Point out each Plasmodium parasite and each leukocyte.
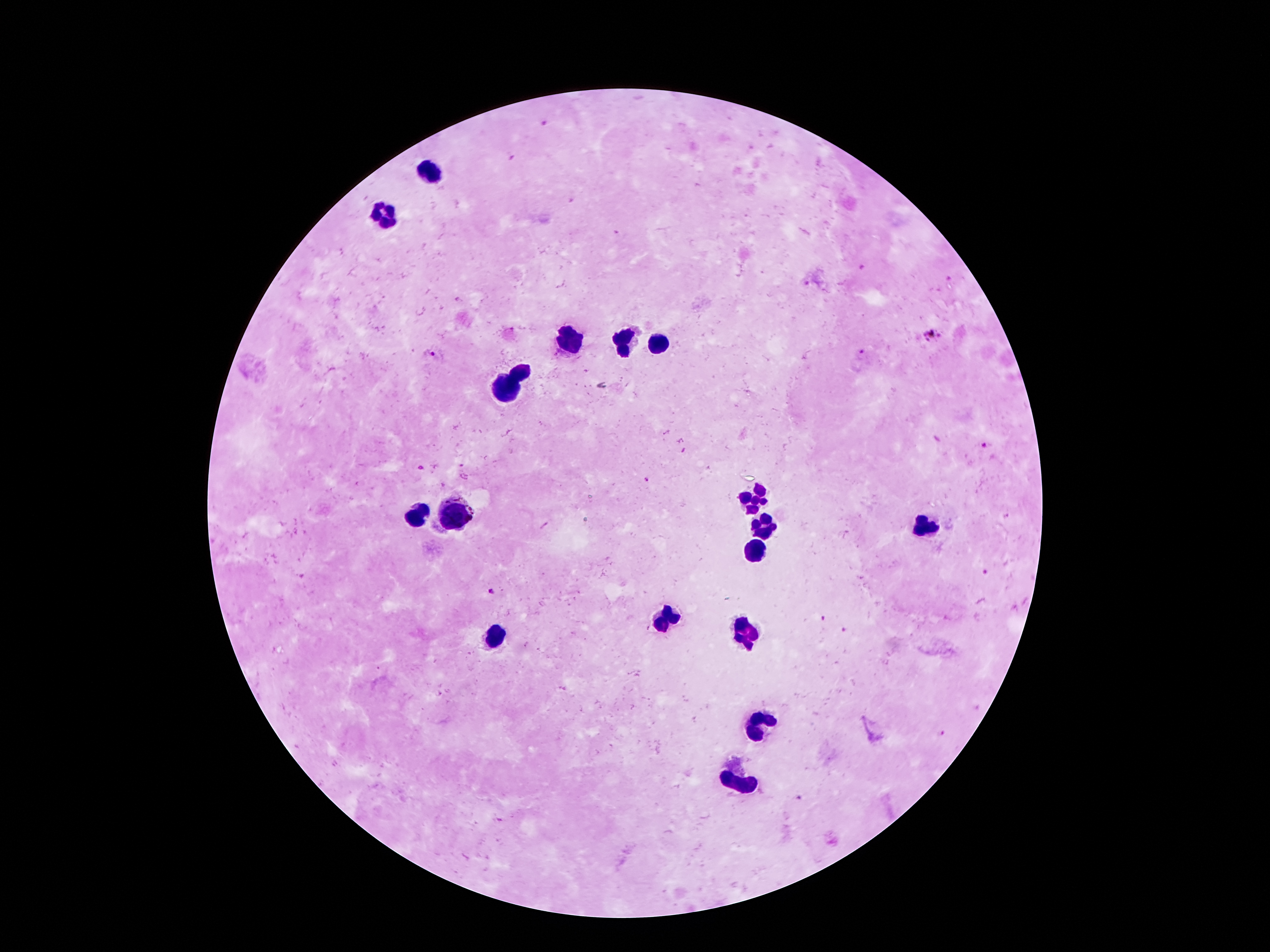

Approximate centers as [x, y] in pixels.
Plasmodium parasites: [542, 123], [513, 156], [618, 235], [933, 336], [861, 352], [432, 354], [985, 446], [421, 468], [648, 481], [987, 573], [491, 592], [822, 619], [843, 630], [941, 733], [797, 798].
Leukocytes: [429, 174], [387, 217], [568, 342], [624, 344], [656, 344], [519, 373], [505, 389], [754, 501], [417, 516], [454, 517], [926, 526], [764, 527], [754, 551], [664, 620], [748, 635], [495, 639], [758, 720], [742, 782].

image size = 1270×952 pixels
capture = smartphone through the microscope eyepiece
magnification = 100x
patient malaria status = positive for Plasmodium falciparum
preparation = thick blood film
field of view = one from this slide
stain = Giemsa